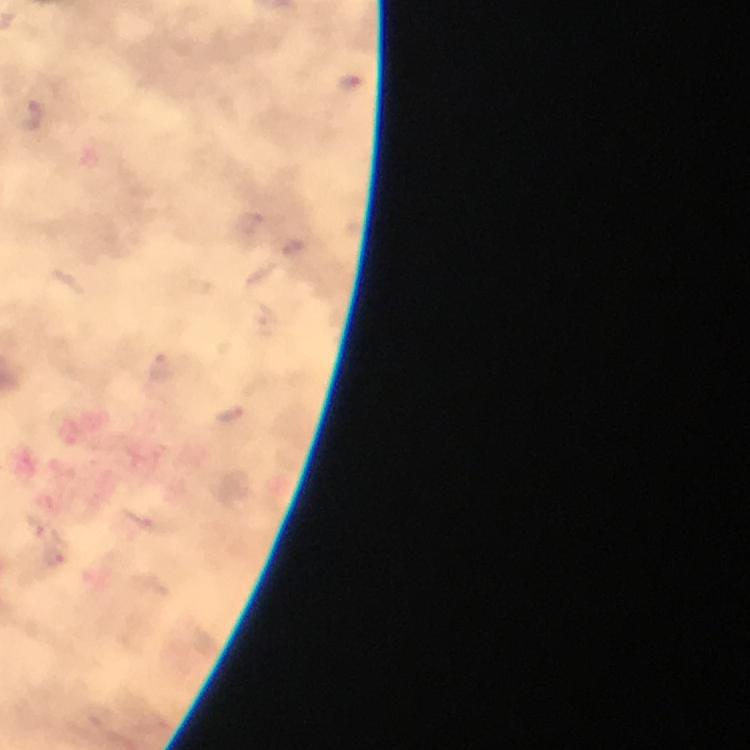
Approximate centers as {x, y} in pixels. Plasmodium parasite locations: {25, 112}, {52, 557}. Image is 750×750 pixels. Photographed with a smartphone mounted on the microscope. Immersion oil was used. Giemsa-stained preparation. A crop from one field of view. From a diagnostic examination for malaria. 100x magnification. Thick smear.